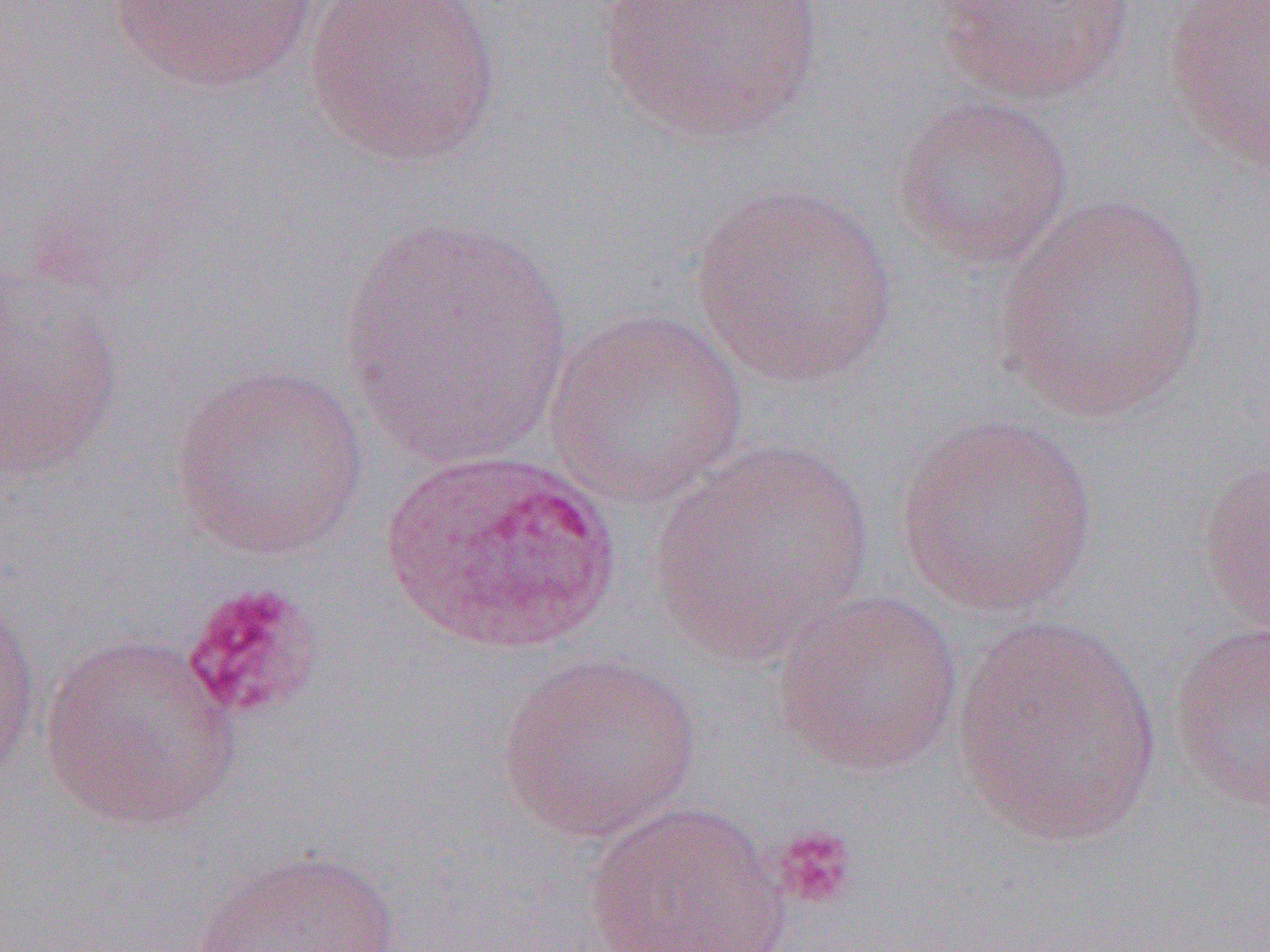

slide-level diagnosis = Plasmodium ovale
magnification = 1000x
preparation = thin blood smear
platelet locations = approximate bounding boxes as (x1, y1, x2, y2) in pixels: (180, 580, 323, 724), (771, 826, 859, 910)
field of view = single
image size = 1270×952 pixels
modality = optical microscopy
uninfected red blood cell locations = approximate bounding boxes as (x1, y1, x2, y2) in pixels: (101, 0, 332, 95), (304, 0, 503, 169), (597, 0, 824, 146), (932, 0, 1136, 104), (1163, 1, 1270, 173), (891, 92, 1075, 270), (690, 181, 898, 389), (992, 193, 1212, 422), (337, 215, 574, 468), (1, 257, 124, 479), (544, 309, 750, 508), (169, 361, 371, 561), (894, 415, 1100, 618), (647, 440, 875, 663), (1197, 454, 1270, 631), (772, 588, 965, 776), (0, 592, 42, 785), (949, 616, 1166, 848), (1167, 619, 1270, 814), (39, 633, 242, 832), (495, 652, 701, 843), (581, 801, 792, 952), (187, 847, 413, 952)
Plasmodium ovale-infected red blood cell locations = approximate bounding boxes as (x1, y1, x2, y2) in pixels: (378, 448, 622, 655)